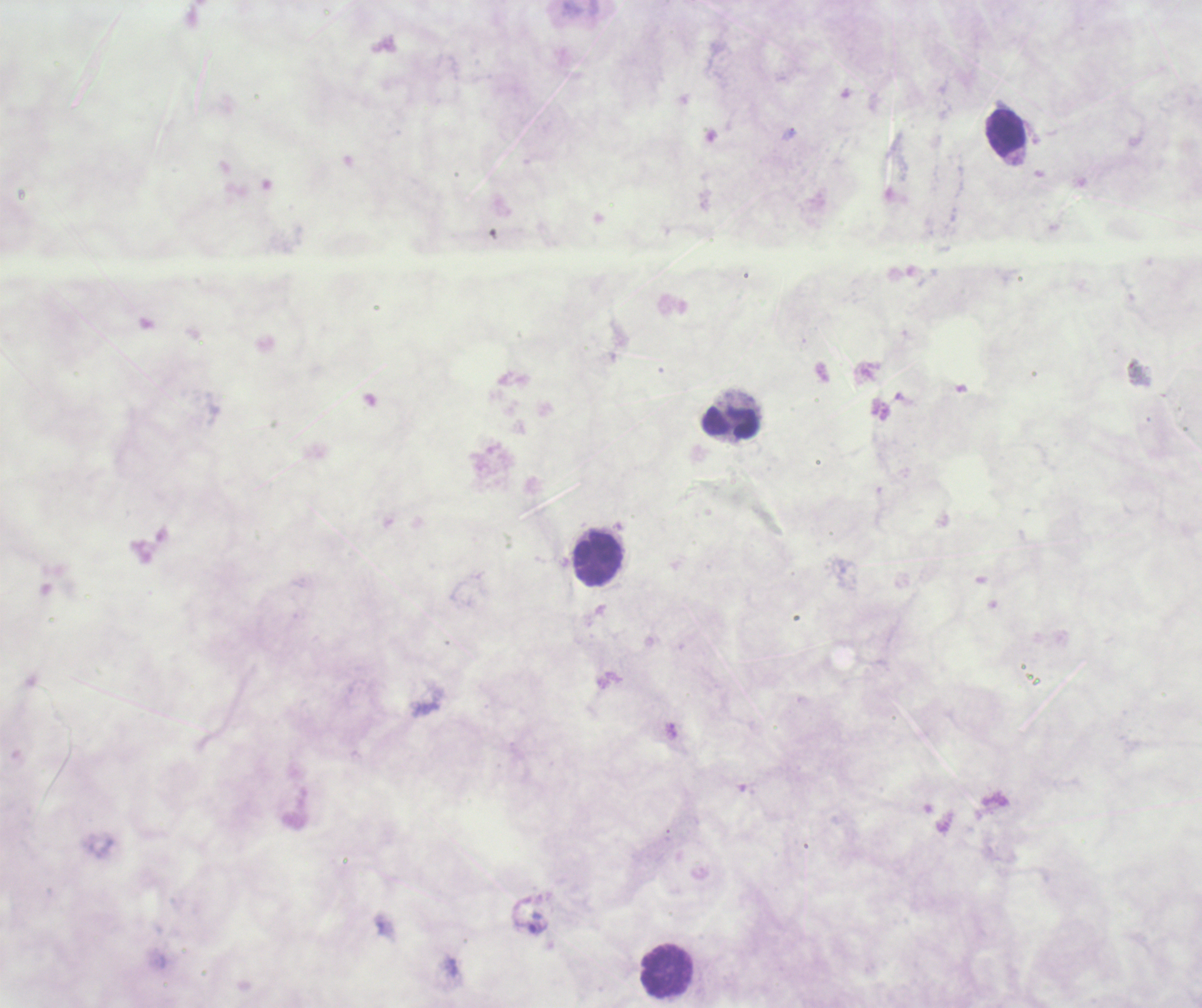

Approximate centers as (x, y) in pixels.
Summary:
  - Leukocyte locations: (1006, 133), (730, 422), (597, 557), (664, 972)
  - Trophozoite locations: (534, 925)
  - Stain: Romanowsky
  - Result: positive for malaria parasites
  - Magnification: 100x
  - Preparation: thick blood film
  - Context: previously used in a real diagnosis
  - Field of view: one from this slide
  - Coloration quality: bad
  - Background quality: unsatisfactory
  - Image size: 1202×1008 pixels